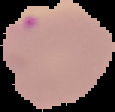
{
  "malaria_status": "parasitized",
  "preparation": "thin blood film",
  "image_type": "cell region segmented out of the field of view; surrounding area masked to black",
  "image_size": "115×112 pixels"
}